State which cell type is depicted.
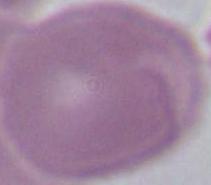
This is an erythrocyte.

modality: micrograph
magnification: 1000x